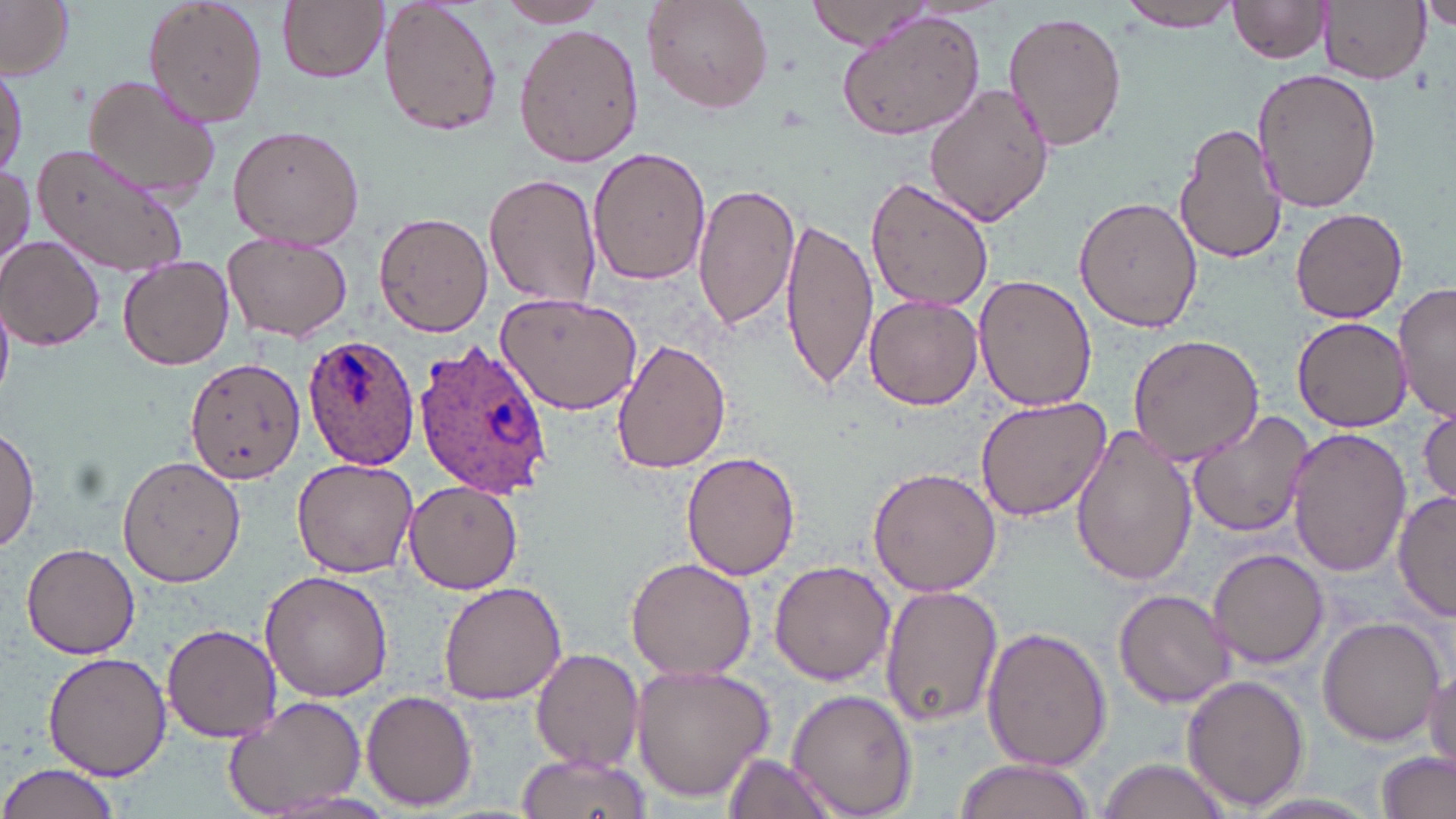

Summary:
  - Coordinate format: approximate bounding boxes as [x1, y1, x2, y2] in pixels
  - Uninfected red blood cell locations: [142, 0, 269, 128], [278, 0, 388, 84], [378, 0, 503, 138], [641, 0, 775, 115], [806, 0, 942, 50], [1116, 0, 1245, 34], [1228, 0, 1335, 64], [0, 1, 76, 78], [497, 1, 613, 28], [1422, 1, 1455, 34], [1318, 2, 1427, 85], [835, 7, 987, 142], [1002, 12, 1129, 152], [513, 21, 643, 167], [0, 64, 24, 185], [1251, 68, 1383, 214], [83, 73, 225, 206], [924, 84, 1056, 227], [1174, 122, 1286, 266], [227, 125, 366, 250], [29, 140, 196, 280], [586, 146, 711, 286], [0, 160, 32, 279], [486, 170, 603, 311], [865, 175, 995, 314], [692, 182, 801, 333], [1073, 196, 1204, 332], [1288, 208, 1410, 323], [373, 212, 492, 337], [778, 215, 879, 393], [224, 234, 351, 343], [1, 237, 108, 349], [118, 254, 234, 369], [973, 274, 1095, 412], [1392, 285, 1455, 420], [864, 292, 983, 410], [495, 293, 643, 415], [1291, 317, 1410, 431], [1126, 333, 1264, 464], [612, 340, 731, 474], [185, 357, 306, 485], [975, 394, 1114, 520], [1416, 405, 1456, 513], [1186, 410, 1316, 539], [0, 425, 40, 555], [1068, 425, 1197, 586], [1286, 426, 1411, 579], [680, 451, 801, 580], [118, 455, 246, 587], [290, 458, 417, 577], [868, 466, 1001, 597], [404, 477, 525, 594], [1393, 489, 1456, 622], [20, 542, 142, 660], [1207, 547, 1328, 670], [626, 557, 755, 681], [768, 560, 894, 684], [260, 570, 392, 702], [438, 579, 566, 703], [877, 583, 1005, 728], [1114, 589, 1236, 711], [1317, 615, 1446, 747], [161, 622, 282, 742], [981, 627, 1112, 772], [531, 648, 644, 770], [43, 650, 171, 779], [1426, 658, 1455, 777], [629, 659, 775, 800], [1182, 673, 1310, 812], [787, 689, 918, 817], [361, 690, 479, 810], [223, 694, 366, 816], [1378, 749, 1454, 819], [517, 750, 650, 819], [722, 753, 838, 818], [1094, 757, 1236, 819], [952, 759, 1101, 819], [0, 764, 122, 819], [1237, 794, 1385, 819]
  - Plasmodium ovale-infected red blood cell locations: [301, 334, 419, 469], [416, 342, 554, 500]
  - Slide-level diagnosis: Plasmodium ovale
  - Image size: 1456×819 pixels
  - Preparation: thin blood smear
  - Stain: May-Grünwald-Giemsa
  - Modality: optical microscopy
  - Field of view: one of a larger specimen
  - Magnification: 1000x